Describe the morphology of the erythrocytes.
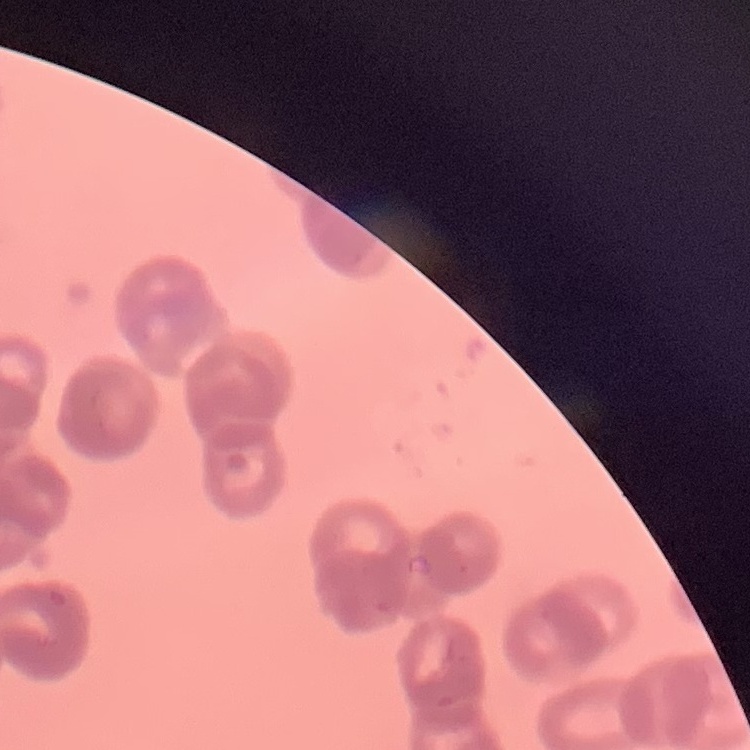

They show rouleaux formation.

preparation: thin blood smear
image_type: square crop of a larger photomicrograph
stain: Field's or Giemsa